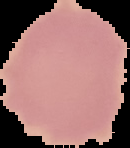
preparation = thin blood smear
image type = segmented cell region with the area outside set to black
malaria status = uninfected
image size = 130×148 pixels